Outline each uninfected red blood cell.
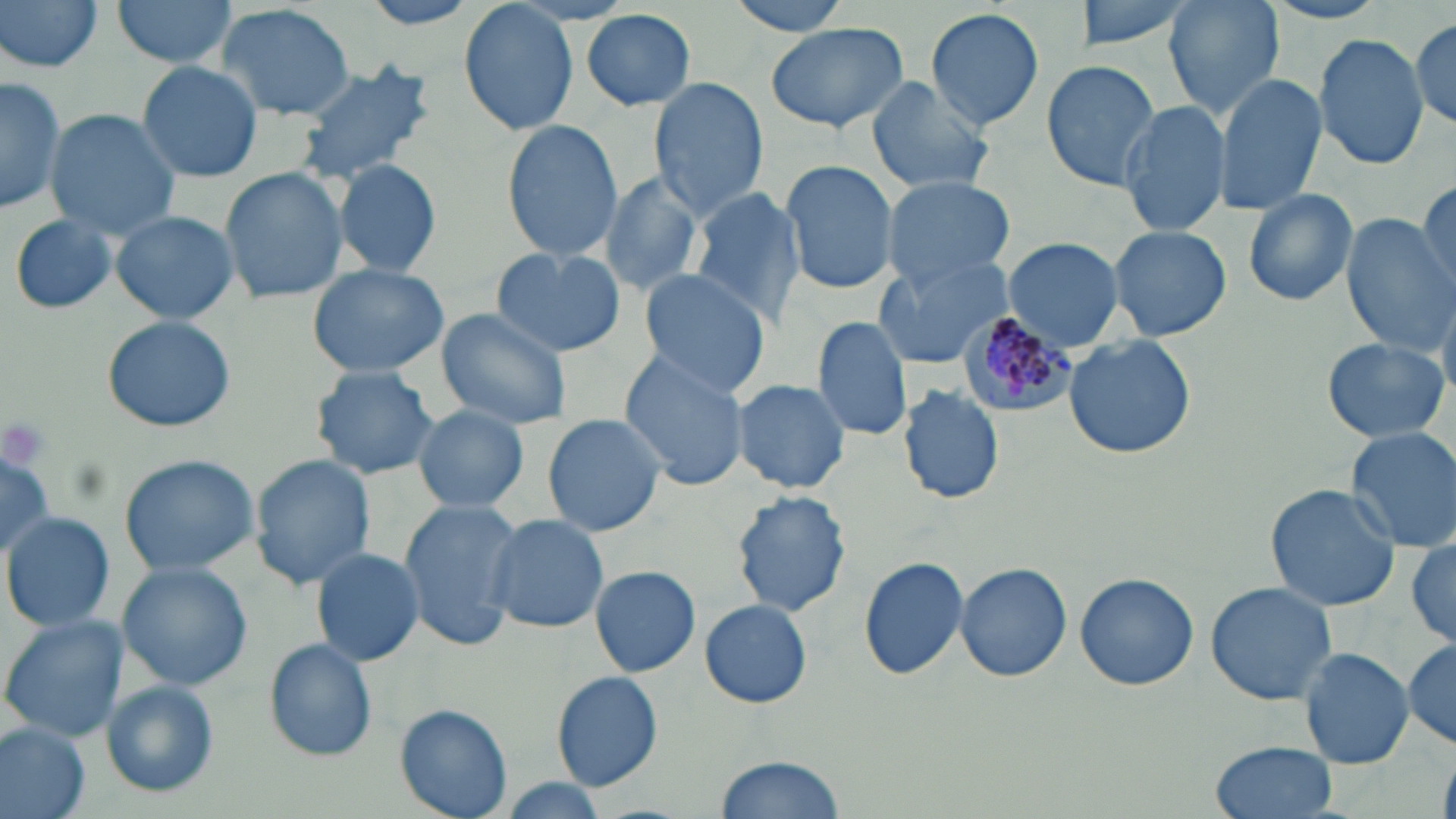

Approximate bounding boxes as (x1,y1)-(x2,y2) corner pairs in pixels.
Uninfected red blood cells: (1,0)-(105,73), (111,0)-(238,69), (356,0)-(492,32), (725,0)-(856,35), (1074,0)-(1196,52), (1165,0)-(1281,117), (459,2)-(580,138), (219,3)-(355,120), (926,6)-(1046,132), (582,10)-(696,111), (1410,16)-(1456,130), (765,22)-(910,133), (1312,31)-(1430,171), (1040,59)-(1164,189), (292,60)-(436,188), (136,61)-(262,182), (1213,71)-(1326,215), (0,76)-(66,214), (866,76)-(996,195), (648,77)-(770,218), (1117,99)-(1234,239), (44,110)-(181,239), (502,120)-(623,261), (332,157)-(443,279), (780,161)-(900,294), (220,168)-(348,304), (599,174)-(703,297), (1418,175)-(1454,295), (880,176)-(1017,285), (689,188)-(806,324), (1242,188)-(1359,306), (111,209)-(239,324), (9,214)-(119,316), (1343,215)-(1451,354), (1107,224)-(1232,342), (1002,236)-(1126,350), (489,247)-(626,356), (871,254)-(1014,370), (306,263)-(449,379), (636,269)-(773,398), (435,308)-(573,430), (102,315)-(236,432), (811,316)-(912,442), (1063,334)-(1197,460), (1321,336)-(1450,445), (621,352)-(751,491), (309,365)-(441,480), (731,378)-(852,493), (898,385)-(1005,504), (412,404)-(529,513), (541,413)-(667,536), (1345,427)-(1456,552), (0,446)-(56,564), (117,454)-(261,576), (251,455)-(375,589), (1265,483)-(1401,611), (731,490)-(851,617), (398,499)-(522,646), (3,512)-(113,633), (484,514)-(610,634), (1407,536)-(1456,650), (310,545)-(426,667), (859,555)-(970,682), (116,561)-(254,690), (954,562)-(1072,682), (589,565)-(700,678), (1073,571)-(1200,691), (1206,582)-(1339,706), (699,599)-(813,708), (1,616)-(126,741), (1403,638)-(1456,748), (263,639)-(377,761), (1300,649)-(1414,769), (551,671)-(664,791), (98,681)-(220,798), (394,703)-(514,819), (0,723)-(89,819), (1209,741)-(1338,819), (714,752)-(847,818).

Plasmodium malariae-infected red blood cell locations: (959,308)-(1079,416). Slide-level diagnosis: Plasmodium malariae. One field of a larger specimen. Thin blood film. Light microscopy. May-Grünwald-Giemsa-stained preparation. 1000x magnification. Image is 1456×819 pixels.